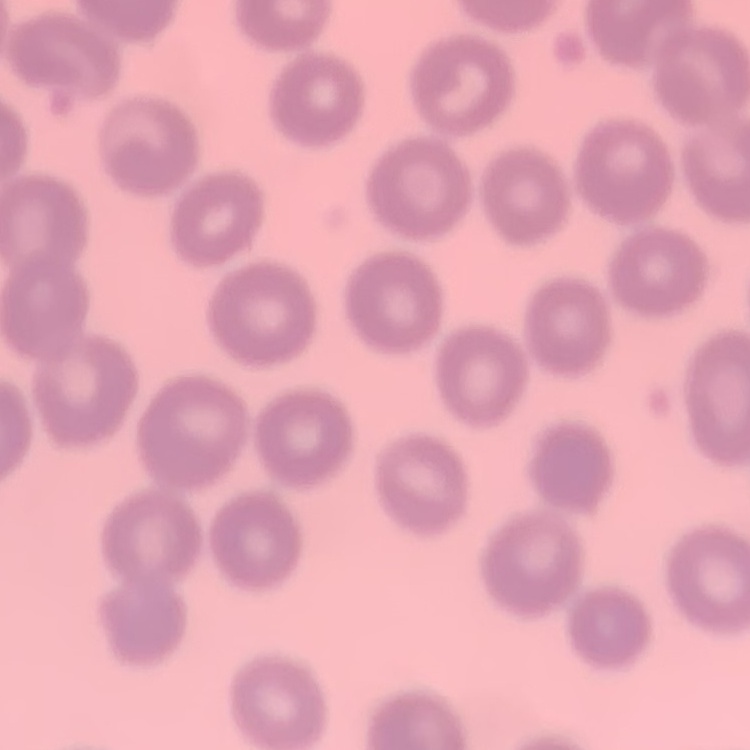
Summary:
  - Erythrocyte morphology: no rouleaux formation
  - Preparation: thin peripheral smear
  - Image type: square crop of a larger photomicrograph
  - Stain: Field's or Giemsa